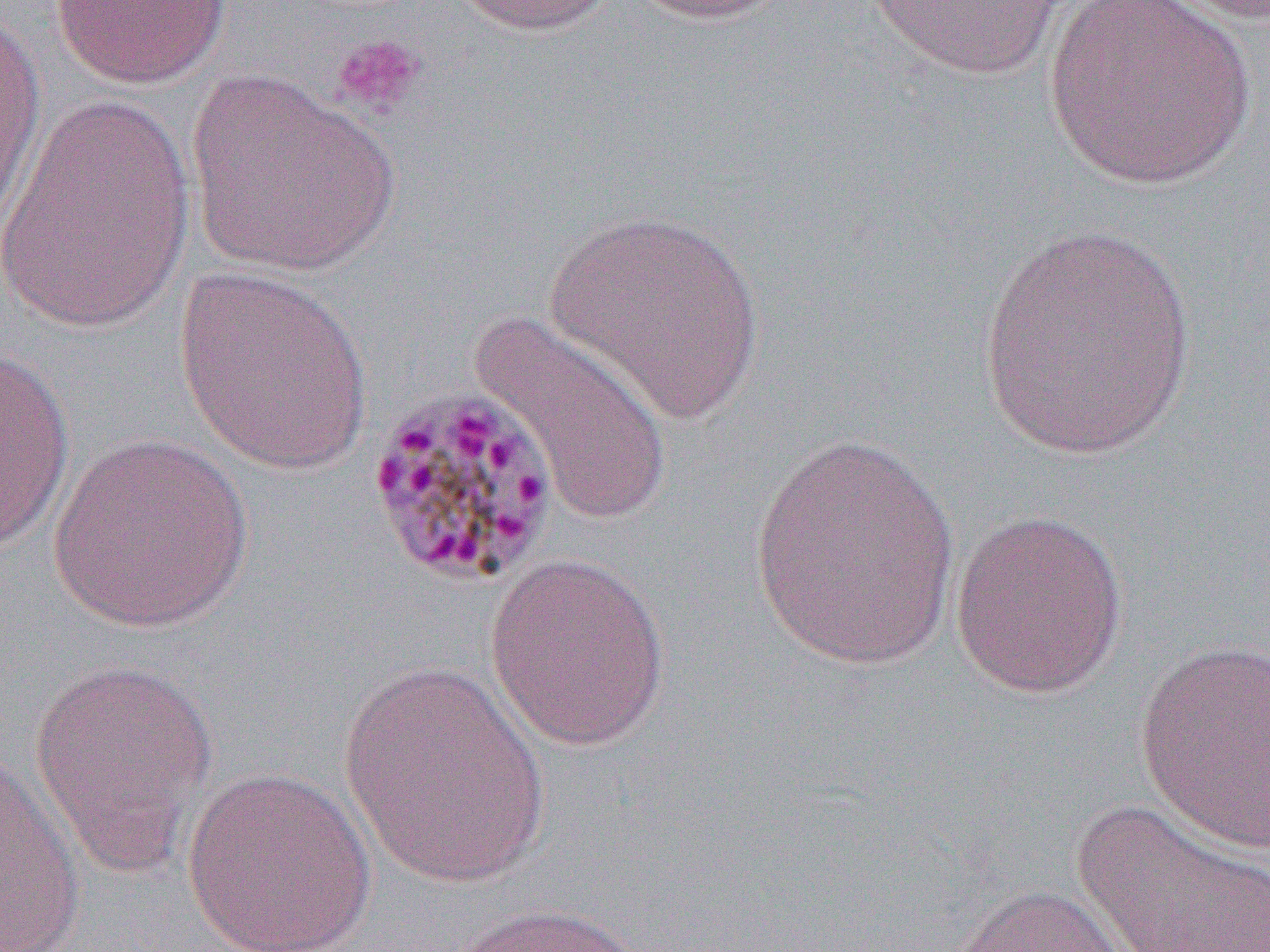 Approximate bounding boxes as [x1, y1, x2, y2] in pixels. Platelet locations: [328, 31, 428, 120]. Uninfected red blood cell locations: [49, 0, 232, 89], [444, 0, 622, 37], [621, 0, 796, 25], [861, 0, 1072, 81], [1145, 0, 1270, 27], [1040, 1, 1259, 190], [0, 6, 46, 236], [186, 72, 400, 277], [0, 90, 196, 335], [544, 207, 766, 425], [974, 224, 1201, 460], [174, 265, 374, 475], [469, 310, 676, 526], [0, 348, 76, 551], [749, 429, 961, 672], [46, 433, 255, 634], [948, 508, 1129, 700], [483, 550, 672, 751], [1134, 638, 1270, 854], [27, 656, 219, 880], [339, 660, 553, 889], [1, 751, 87, 949], [181, 766, 377, 952], [1070, 799, 1270, 952], [950, 883, 1138, 952], [438, 900, 651, 952]. Slide-level diagnosis: Plasmodium malariae. Optical microscopy. Thin blood smear. Captured at 1000x magnification. Image is 1270×952 pixels. Single field of view.